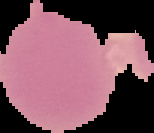

Result: no malaria parasites seen. From a thin blood film. Cell region segmented out of the field of view; the surrounding area is masked to black. Image is 154×133 pixels.